Comment on the morphology of the red blood cells.
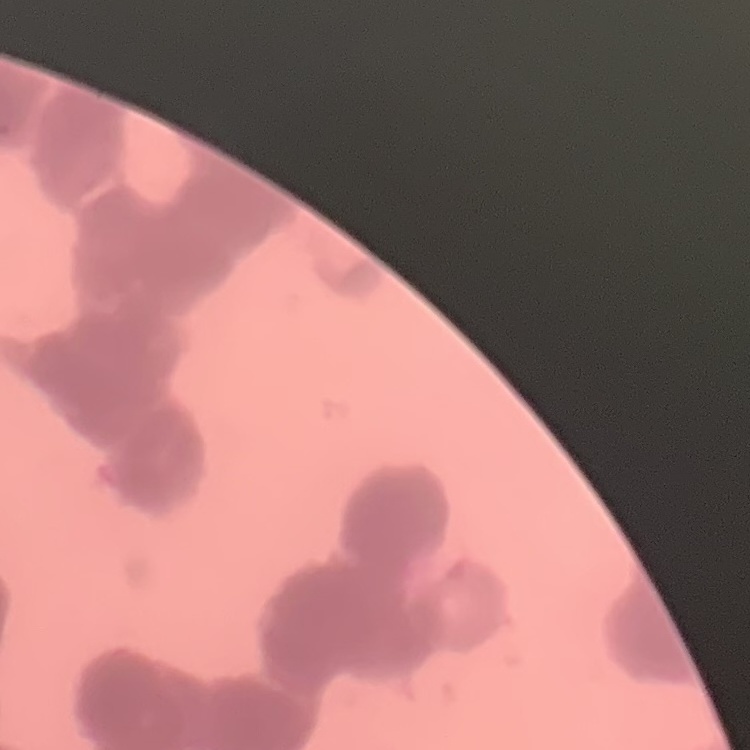
They show rouleaux formation.

image type = square crop of a larger photomicrograph
preparation = thin blood smear
stain = Field's or Giemsa